Give the position of every Plasmodium parasite.
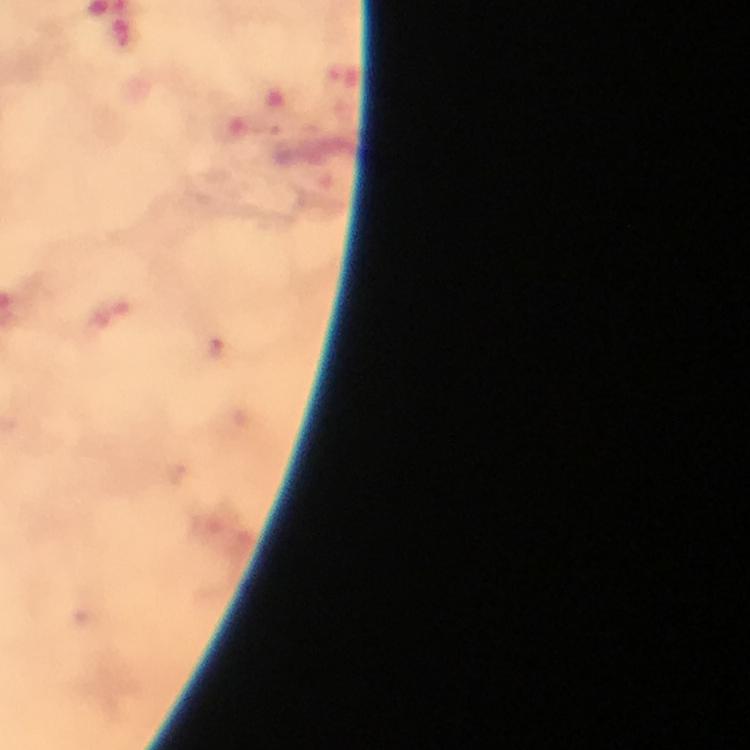
Approximate centers as {x, y} in pixels.
Plasmodium parasites: {214, 348}.

Summary:
  - Capture: smartphone camera through the microscope
  - Image size: 750×750 pixels
  - Magnification: 100x
  - Preparation: thick blood smear
  - Context: from a diagnostic examination for malaria
  - Stain: Giemsa
  - Immersion oil: applied
  - Cropped from: one field of view